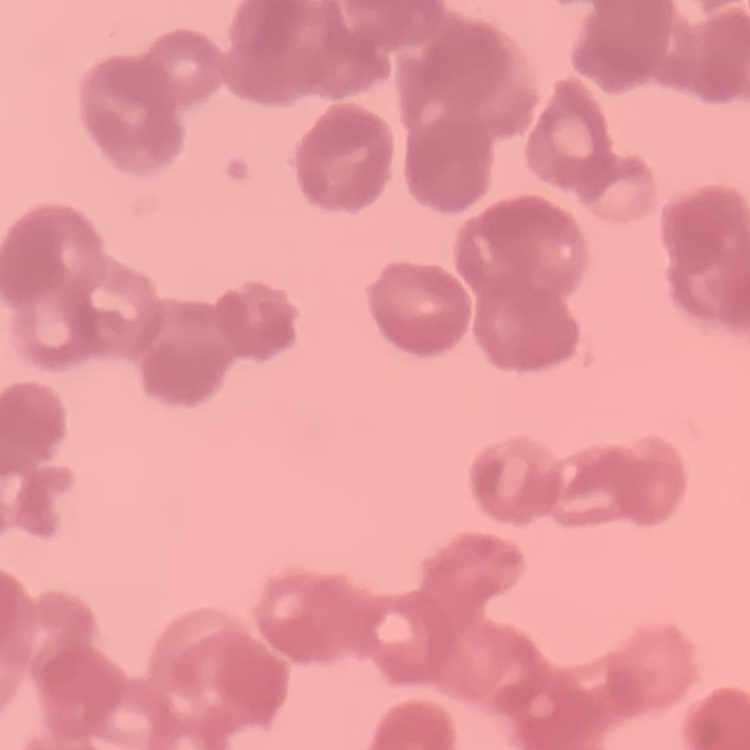 The red blood cells exhibit rouleaux formation. Square crop of a larger photomicrograph. Field's or Giemsa stain. Thin blood film.